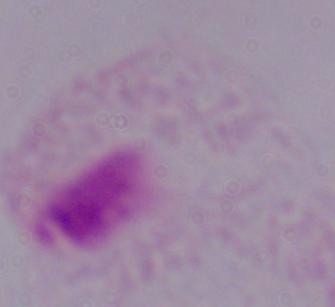

modality = micrograph
identification = trichomonad
magnification = 1000x